Outline each blood parasite and name the species.
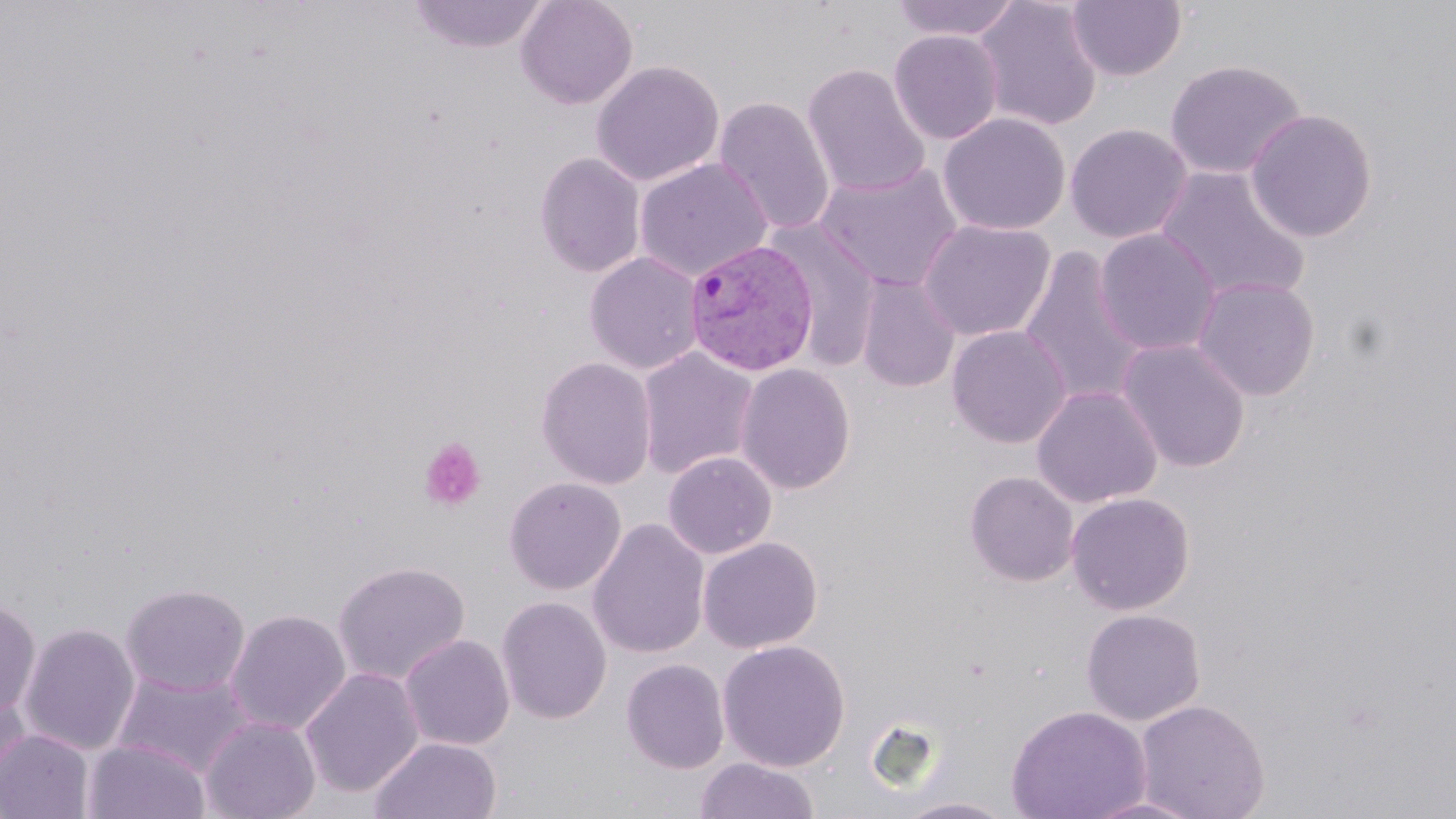

Approximate bounding boxes as (x1,y1)-(x2,y2) corner pairs in pixels.
Plasmodium vivax-infected red blood cells: (685,238)-(820,377).
No Plasmodium falciparum, Plasmodium ovale, Plasmodium malariae, Babesia divergens, or Trypanosoma brucei observed.

slide_level_diagnosis: Plasmodium vivax
platelet_locations: 'approximate bounding boxes as (x1,y1)-(x2,y2) corner pairs in pixels: (418,437)-(487,513)'
stain: May-Grünwald-Giemsa
field_of_view: single
preparation: thin blood film
modality: light microscopy
magnification: 1000x
image_size: 1456×819 pixels
uninfected_red_blood_cell_locations: 'approximate bounding boxes as (x1,y1)-(x2,y2) corner pairs in pixels: (408,0)-(550,53), (516,0)-(638,110), (890,0)-(1023,41), (972,0)-(1103,131), (1066,1)-(1187,81), (888,29)-(1003,144), (1164,59)-(1306,179), (591,60)-(724,186), (802,63)-(930,198), (713,96)-(836,235), (1244,108)-(1378,242), (938,113)-(1070,235), (1065,123)-(1193,244), (534,152)-(646,278), (634,158)-(773,281), (814,162)-(964,292), (1155,165)-(1310,303), (918,219)-(1055,341), (768,221)-(882,371), (1094,228)-(1221,356), (1018,247)-(1148,408), (585,252)-(704,374), (856,275)-(960,393), (1191,277)-(1320,400), (946,324)-(1071,448), (1116,338)-(1252,472), (637,347)-(759,480), (536,357)-(657,490), (735,363)-(856,495), (1031,384)-(1163,508), (663,452)-(777,559), (964,470)-(1079,586), (503,477)-(627,595), (1066,491)-(1195,615), (587,518)-(710,659), (698,536)-(823,653), (332,560)-(471,685), (120,582)-(250,696), (0,597)-(41,719), (496,597)-(612,725), (225,608)-(351,735), (1081,608)-(1205,726), (19,622)-(140,755), (399,634)-(515,751), (717,639)-(851,772), (621,658)-(730,774), (300,667)-(424,799), (111,670)-(254,779), (0,687)-(31,800), (1133,698)-(1270,819), (1006,705)-(1152,819), (200,716)-(321,819), (0,729)-(94,818), (369,736)-(502,819), (83,739)-(210,819), (695,757)-(819,818), (1081,794)-(1208,818), (893,797)-(1019,818)'